Locate every Plasmodium parasite.
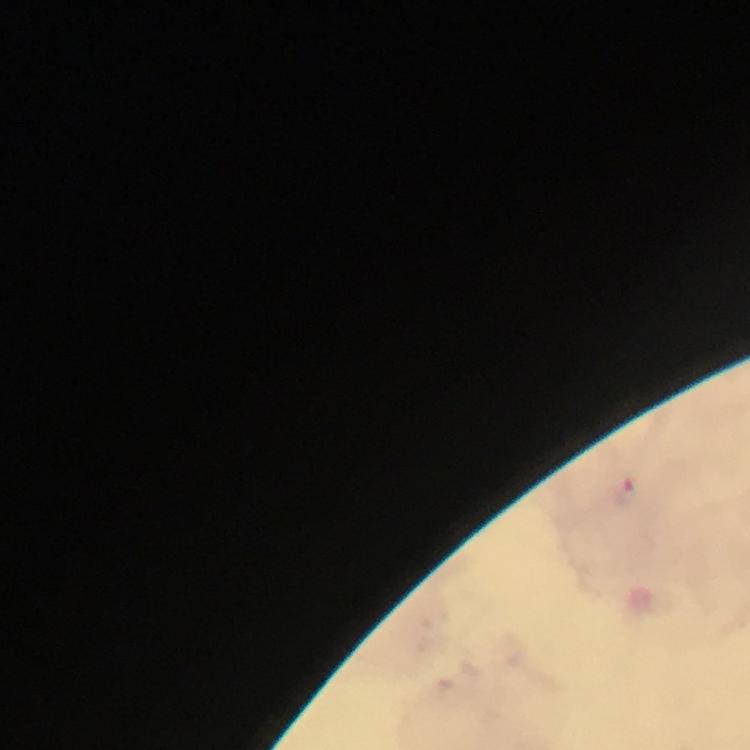

Approximate centers as {x, y} in pixels.
Plasmodium parasites: {625, 496}.

From a diagnostic examination for malaria. Photographed through the microscope with a smartphone camera. Thick blood film. Image is 750×750 pixels. Immersion oil was used. A crop from one field of view. At 100x magnification. Giemsa stain.